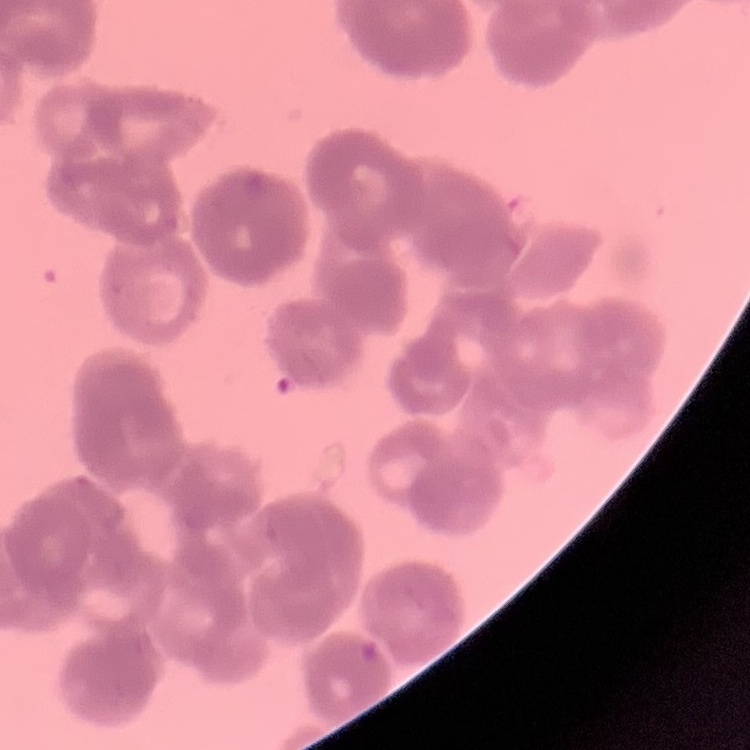
erythrocyte_morphology: rouleaux formation
stain: Field's or Giemsa
image_type: one tile cut from a larger photomicrograph
preparation: thin peripheral smear